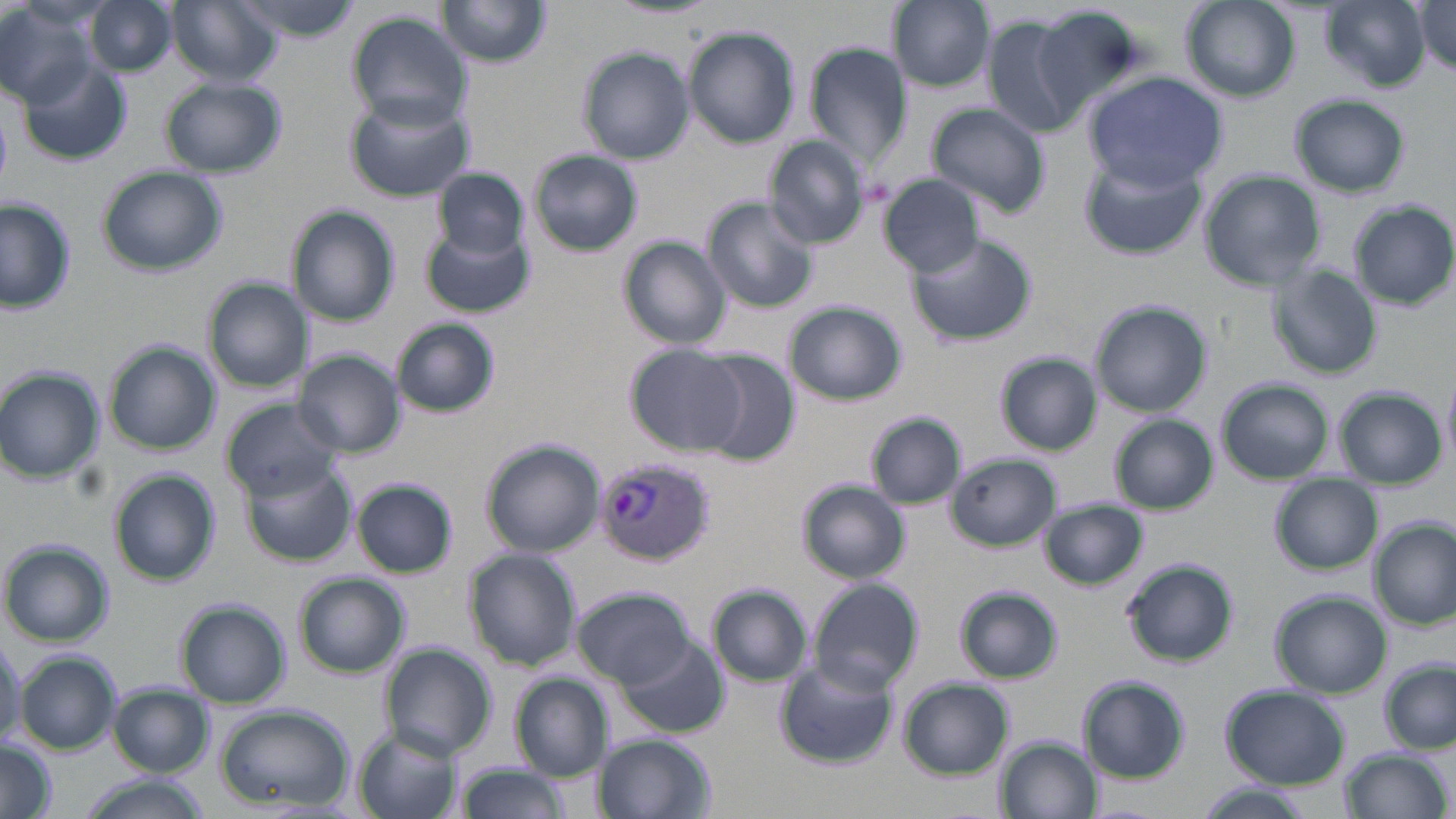

slide-level diagnosis = Plasmodium vivax
image size = 1456×819 pixels
uninfected red blood cell locations = approximate bounding boxes as [x1, y1, x2, y2] in pixels: [88, 0, 175, 76], [167, 0, 282, 87], [229, 0, 363, 40], [610, 0, 720, 21], [890, 0, 994, 91], [1180, 0, 1301, 103], [0, 1, 97, 105], [439, 1, 551, 68], [1320, 1, 1432, 90], [1416, 2, 1456, 71], [1015, 7, 1143, 124], [347, 10, 473, 128], [984, 15, 1086, 138], [684, 27, 799, 148], [807, 45, 911, 171], [578, 48, 695, 164], [18, 55, 132, 166], [1084, 72, 1226, 190], [161, 79, 286, 176], [1291, 93, 1409, 198], [344, 94, 474, 202], [926, 102, 1051, 218], [764, 137, 871, 249], [528, 149, 643, 256], [1077, 153, 1206, 261], [97, 166, 225, 274], [434, 167, 528, 260], [1200, 170, 1326, 290], [881, 176, 987, 277], [0, 196, 78, 314], [703, 198, 817, 311], [1348, 202, 1456, 308], [295, 206, 398, 327], [421, 227, 534, 316], [908, 232, 1036, 347], [619, 238, 732, 348], [1270, 266, 1382, 379], [202, 279, 306, 392], [1090, 300, 1212, 416], [783, 302, 907, 405], [391, 318, 501, 418], [105, 343, 219, 453], [625, 344, 743, 454], [298, 351, 406, 456], [693, 351, 801, 465], [996, 353, 1100, 454], [0, 367, 103, 484], [1442, 369, 1456, 467], [1217, 379, 1333, 483], [1335, 387, 1446, 487], [222, 399, 341, 499], [866, 412, 968, 510], [1111, 415, 1219, 514], [481, 439, 605, 556], [948, 455, 1061, 550], [239, 460, 357, 567], [111, 471, 221, 588], [1269, 476, 1383, 574], [353, 479, 459, 576], [798, 479, 911, 583], [1040, 499, 1148, 591], [1372, 519, 1455, 628], [2, 540, 113, 648], [463, 549, 582, 671], [1123, 558, 1238, 667], [293, 572, 410, 678], [809, 579, 923, 695], [710, 586, 813, 686], [955, 586, 1063, 683], [572, 587, 696, 687], [1271, 590, 1390, 697], [177, 602, 290, 707], [616, 634, 729, 738], [381, 643, 497, 760], [16, 651, 120, 754], [776, 661, 896, 769], [1382, 661, 1456, 753], [512, 675, 612, 779], [897, 678, 1013, 778], [1082, 678, 1192, 781], [109, 685, 213, 776], [1220, 685, 1350, 790], [214, 704, 354, 811], [353, 729, 462, 819], [593, 733, 716, 819], [997, 736, 1097, 819], [0, 741, 57, 819], [1339, 747, 1450, 819], [456, 762, 573, 819], [77, 777, 211, 819], [1196, 786, 1309, 819]
magnification = 1000x
preparation = thin blood film
modality = optical microscopy
field of view = one of a larger specimen
stain = May-Grünwald-Giemsa
Plasmodium vivax-infected red blood cell locations = approximate bounding boxes as [x1, y1, x2, y2] in pixels: [592, 457, 716, 568]